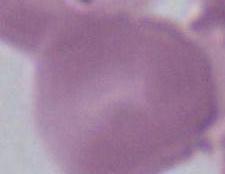

identification: red blood cell
modality: photomicrograph
magnification: 1000x